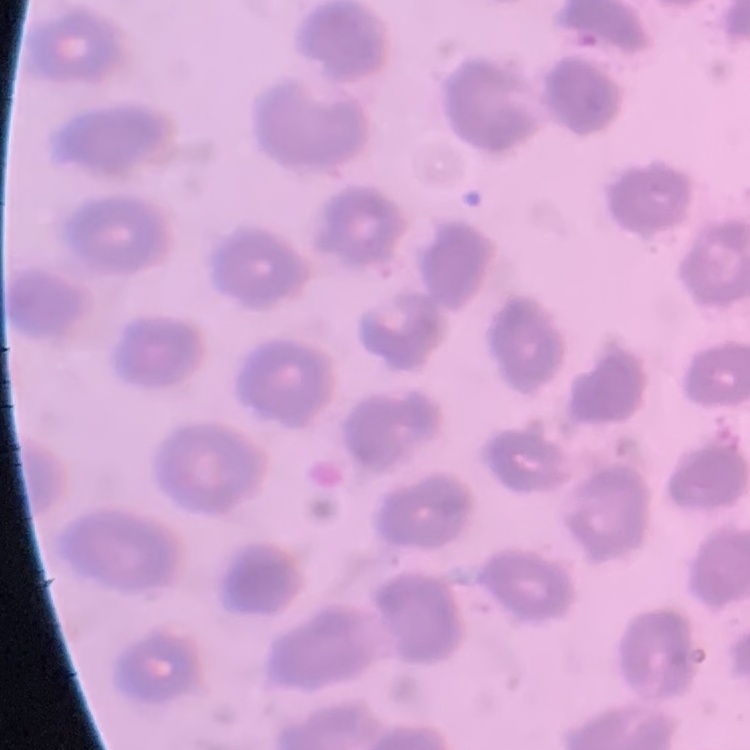
{
  "erythrocyte_morphology": "no rouleaux formation",
  "stain": "Field's or Giemsa",
  "preparation": "thin peripheral smear",
  "image_type": "one tile cut from a larger photomicrograph"
}